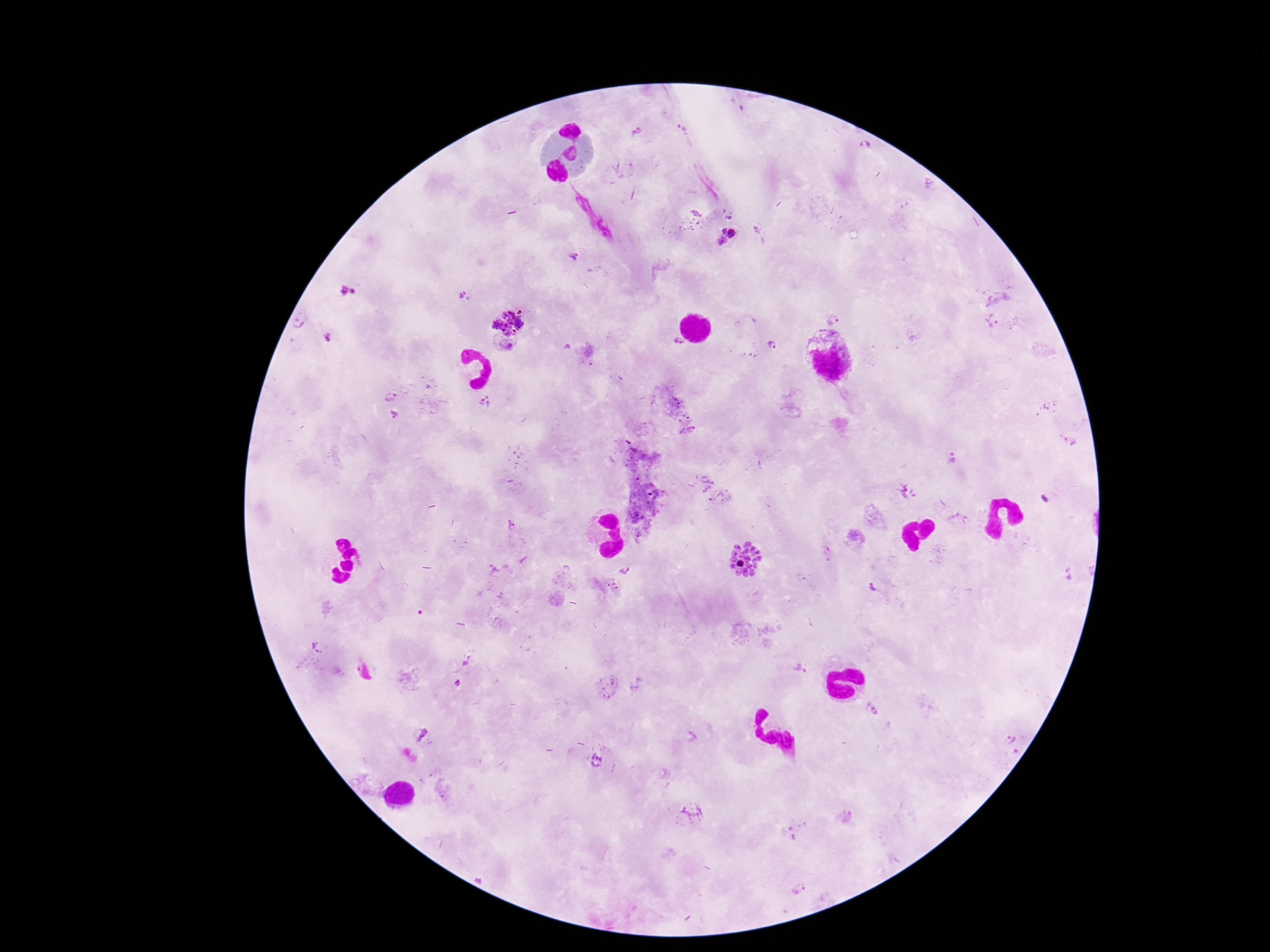
magnification = 100x
stain = Giemsa
field of view = single
capture = smartphone camera through the microscope eyepiece
preparation = thick blood film
image size = 1270×952 pixels
patient malaria status = positive
Plasmodium parasite locations = approximate centers as (x, y) in pixels: (637, 131), (682, 131), (866, 147), (729, 216), (755, 229), (723, 231), (733, 234), (723, 241), (571, 255), (349, 291), (466, 297), (833, 318), (508, 320), (993, 321), (328, 337), (677, 343), (508, 345), (773, 348), (390, 396), (486, 401), (395, 414), (1068, 441), (952, 458), (907, 492), (1045, 498), (511, 525), (638, 535), (744, 558), (624, 569), (1068, 575), (612, 585), (874, 588), (319, 646), (466, 660), (800, 668), (457, 682), (874, 710), (421, 734), (1009, 739), (596, 761), (692, 812), (800, 887)